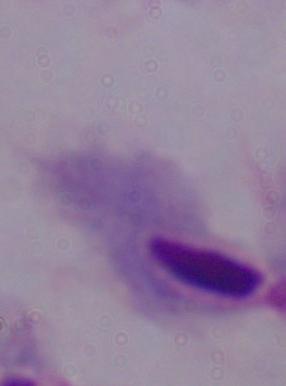
Micrograph. A trichomonad is seen. Captured at 1000x magnification.